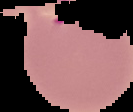

image type = segmented cell region on a black background
preparation = thin blood smear
result = Plasmodium parasites identified
image size = 133×112 pixels